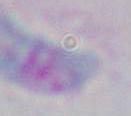

Summary:
  - Modality: photomicrograph
  - Identification: Toxoplasma gondii
  - Magnification: 1000x